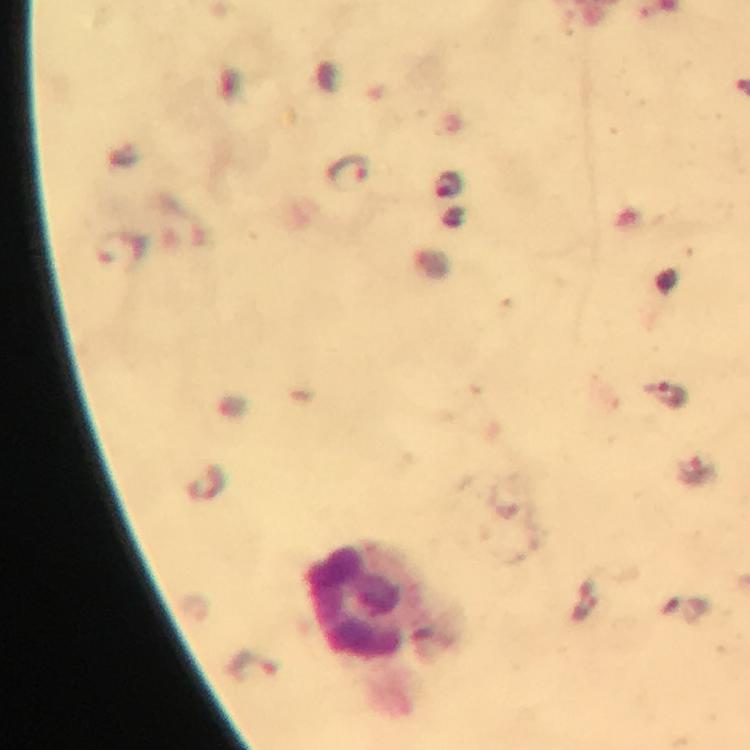
{
  "stain": "Giemsa",
  "magnification": "100x",
  "capture": "smartphone mounted on the microscope",
  "leukocyte_locations": "approximate object centers, in pixels from the top-left corner: (x=358, y=604)",
  "immersion_oil": "used",
  "image_size": "750×750 pixels",
  "cropped_from": "one field of view",
  "context": "from a malaria diagnostic workup",
  "preparation": "thick blood smear",
  "malaria_parasite_locations": "approximate object centers, in pixels from the top-left corner: (x=349, y=168), (x=449, y=185), (x=119, y=248), (x=671, y=393), (x=253, y=666)"
}